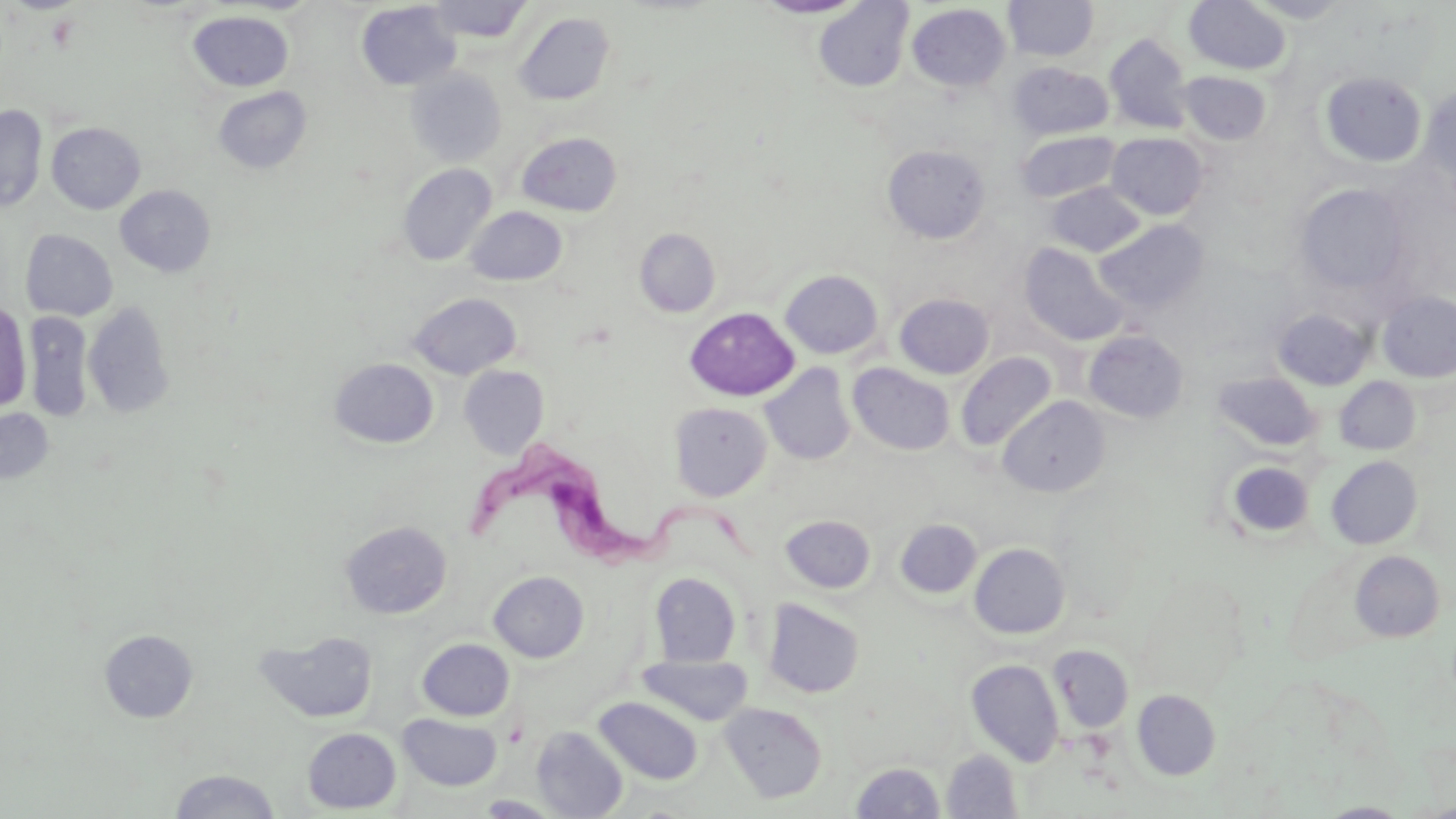

{
  "slide_level_diagnosis": "Trypanosoma brucei",
  "uninfected_red_blood_cell_locations": "approximate bounding boxes as (x1,y1)-(x2,y2) corner pairs in pixels: (753,0)-(865,19), (1184,0)-(1292,75), (427,1)-(532,42), (814,1)-(913,91), (1004,1)-(1098,61), (1244,1)-(1356,24), (356,2)-(461,90), (907,3)-(1010,91), (513,11)-(616,106), (188,12)-(294,91), (1104,33)-(1194,133), (1009,62)-(1113,140), (406,69)-(506,166), (1178,71)-(1272,146), (1320,71)-(1427,168), (1420,84)-(1456,200), (213,86)-(312,174), (0,105)-(47,212), (46,122)-(146,214), (517,131)-(622,216), (1016,131)-(1121,202), (1107,133)-(1208,220), (882,144)-(991,243), (398,163)-(497,266), (1045,182)-(1145,257), (1294,183)-(1411,296), (115,185)-(216,277), (465,206)-(567,285), (1095,219)-(1209,315), (635,228)-(721,317), (21,229)-(118,321), (1019,242)-(1131,346), (780,269)-(883,359), (1376,290)-(1456,382), (409,292)-(521,379), (895,293)-(994,379), (0,301)-(32,412), (83,301)-(174,418), (685,307)-(799,401), (1272,308)-(1372,390), (24,311)-(94,421), (1084,330)-(1188,423), (955,352)-(1057,451), (330,358)-(438,448), (848,363)-(955,455), (760,364)-(856,466), (459,366)-(548,458), (1213,371)-(1320,450), (1335,376)-(1420,455), (998,396)-(1109,497), (669,402)-(771,501), (0,408)-(54,485), (1326,455)-(1423,550), (1224,460)-(1314,540), (781,515)-(875,593), (896,519)-(982,599), (340,521)-(452,619), (968,543)-(1070,638), (1349,550)-(1444,642), (489,571)-(588,662), (650,572)-(741,667), (763,599)-(864,699), (99,629)-(198,722), (255,629)-(379,724), (417,638)-(514,720), (1048,644)-(1133,732), (637,654)-(753,726), (966,659)-(1064,766), (1133,689)-(1221,780), (594,696)-(703,784), (719,702)-(827,803), (398,713)-(502,791), (531,726)-(628,818), (303,727)-(401,813), (942,749)-(1022,818), (850,761)-(946,818), (168,769)-(281,818), (475,795)-(566,817), (1317,802)-(1412,818)",
  "preparation": "thin blood smear",
  "modality": "light microscopy",
  "magnification": "1000x",
  "trypanosoma_brucei_locations": "approximate bounding boxes as (x1,y1)-(x2,y2) corner pairs in pixels: (462,447)-(747,586)",
  "image_size": "1456×819 pixels",
  "stain": "May-Grünwald-Giemsa",
  "field_of_view": "single"
}